Assess the morphology of the erythrocytes.
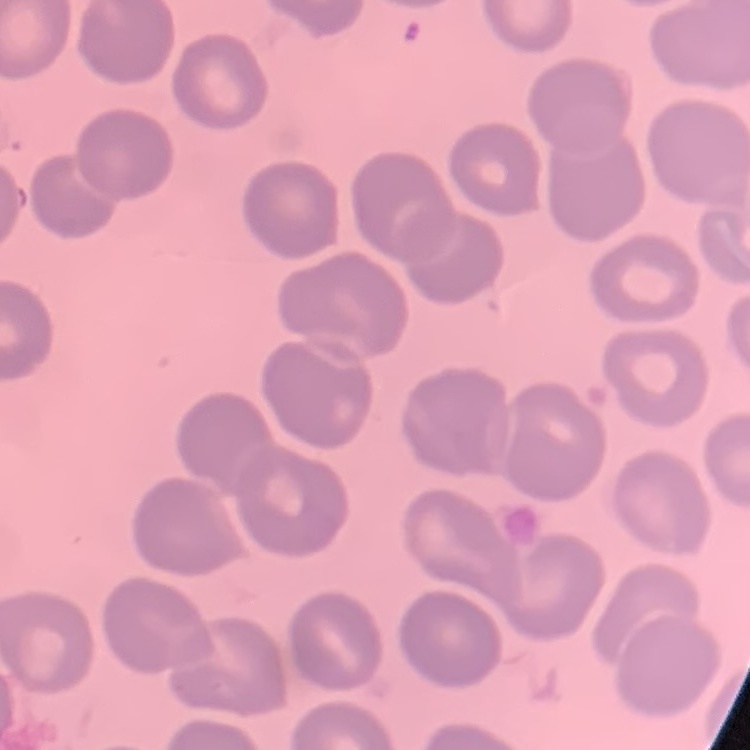
They show no rouleaux formation.

Summary:
  - Stain: Field's or Giemsa
  - Image type: square crop of a larger photomicrograph
  - Preparation: thin blood film